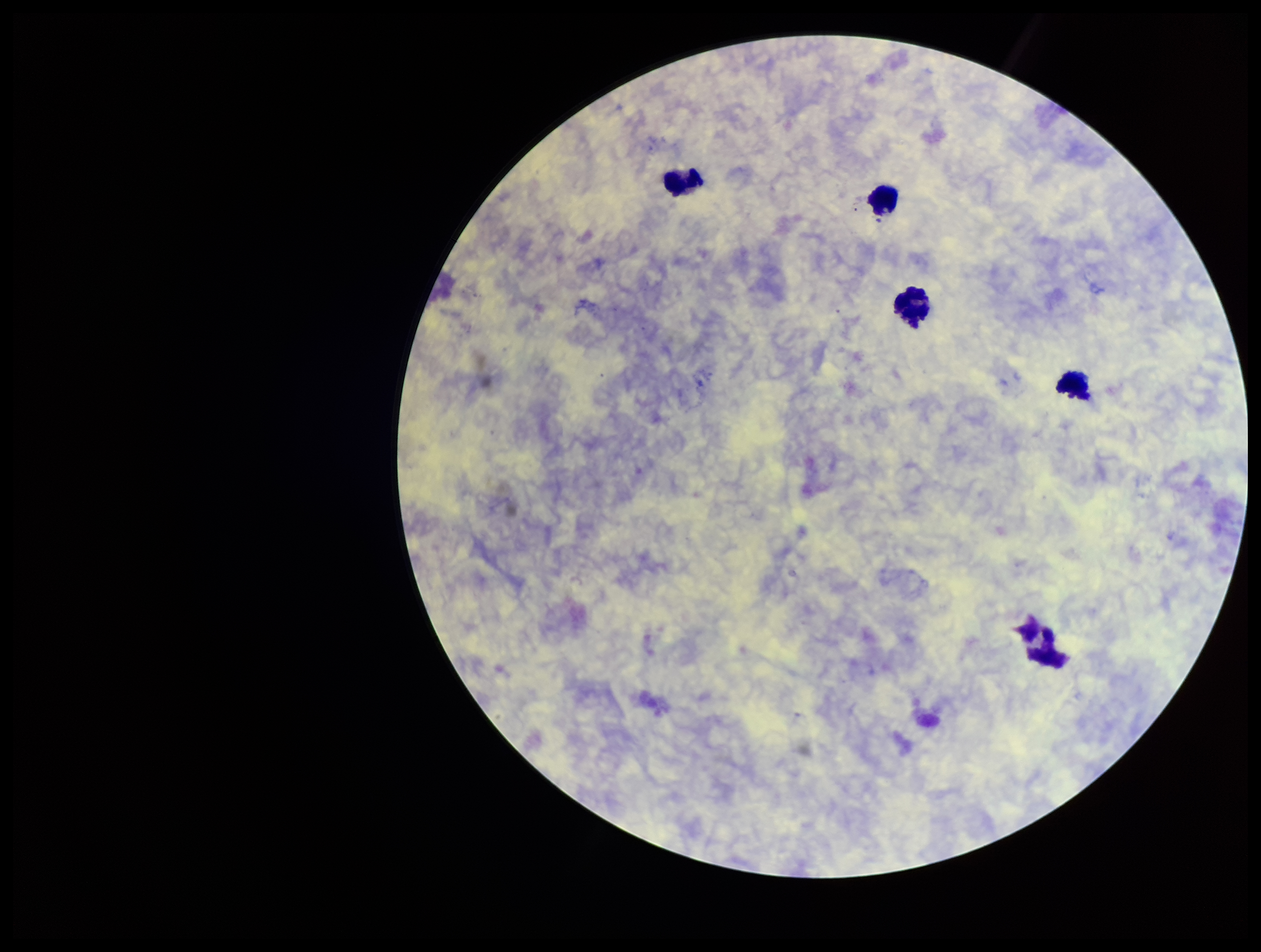
Image is 1261×952 pixels. Leukocyte count: 5. Smartphone photograph taken through the eyepiece of a microscope. Parasite count: 0. Patient malaria status: negative. Plasmodium parasites: none identified. Giemsa stain. Preparation: thick smear. One field from this slide.